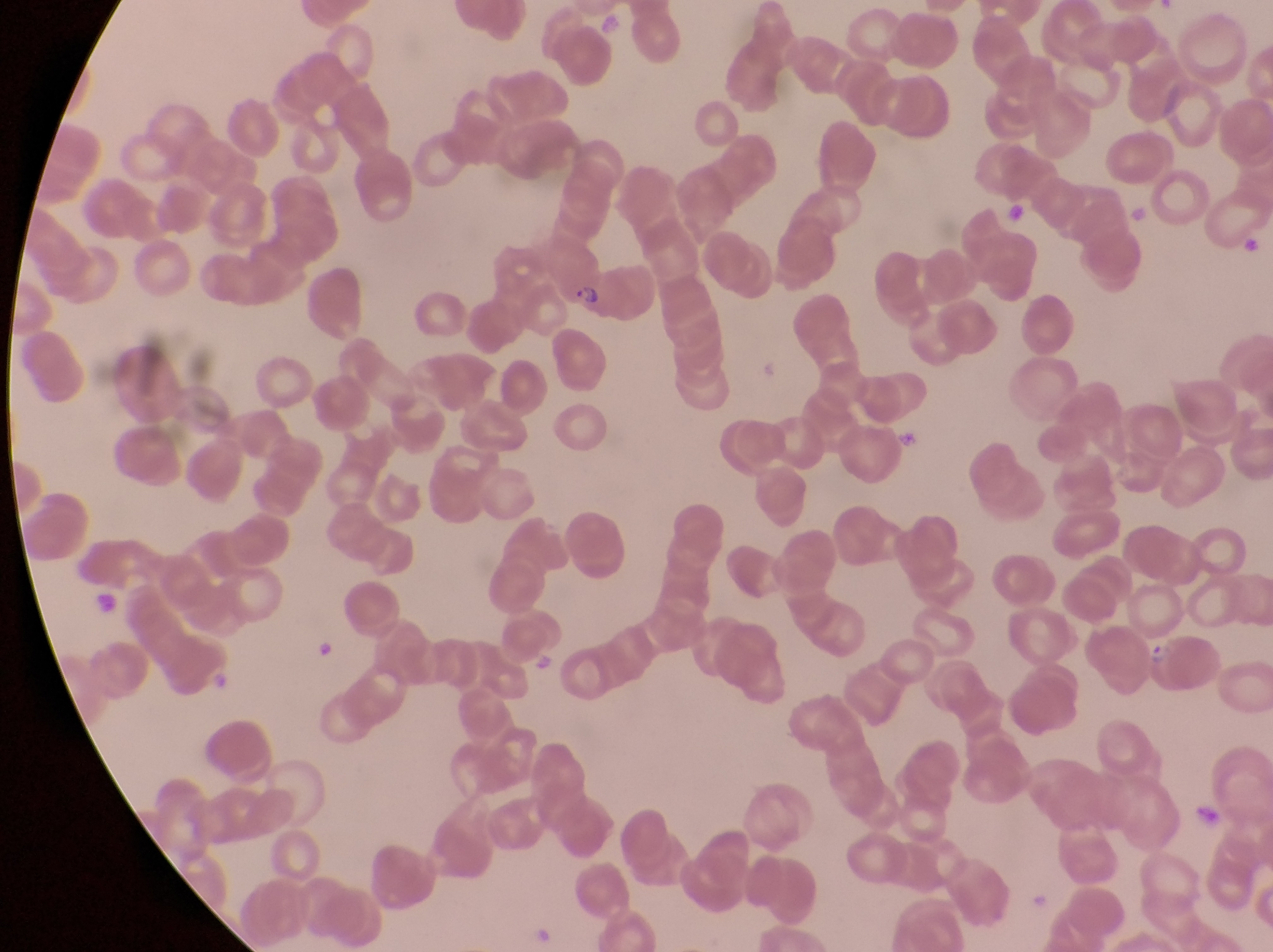
Approximate bounding boxes as [left, top, right, bottom] in pixels. Parasitised red blood cell locations: [535, 232, 610, 310]. Artifact (platelet-like body, stain precipitate, or debris) locations: [1005, 202, 1031, 229], [1131, 202, 1151, 223], [1242, 231, 1269, 260], [897, 426, 928, 462], [93, 589, 125, 616], [317, 636, 341, 664]. Trophozoite locations: [1148, 635, 1171, 675]. One field of view. Photographed through the eyepiece of an Olympus CX-23 microscope with a smartphone camera. At a magnification of 1000x. Image is 1273×952 pixels. Thin blood smear. Collected in Uganda.